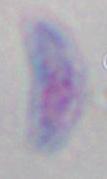
magnification = 1000x
modality = micrograph
identification = Toxoplasma gondii